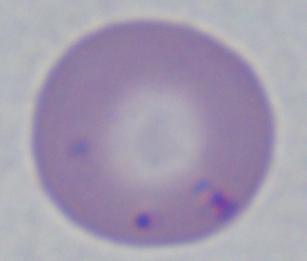
Summary:
  - Identification: Babesia
  - Magnification: 1000x
  - Modality: photomicrograph